Identify the blood parasite species.
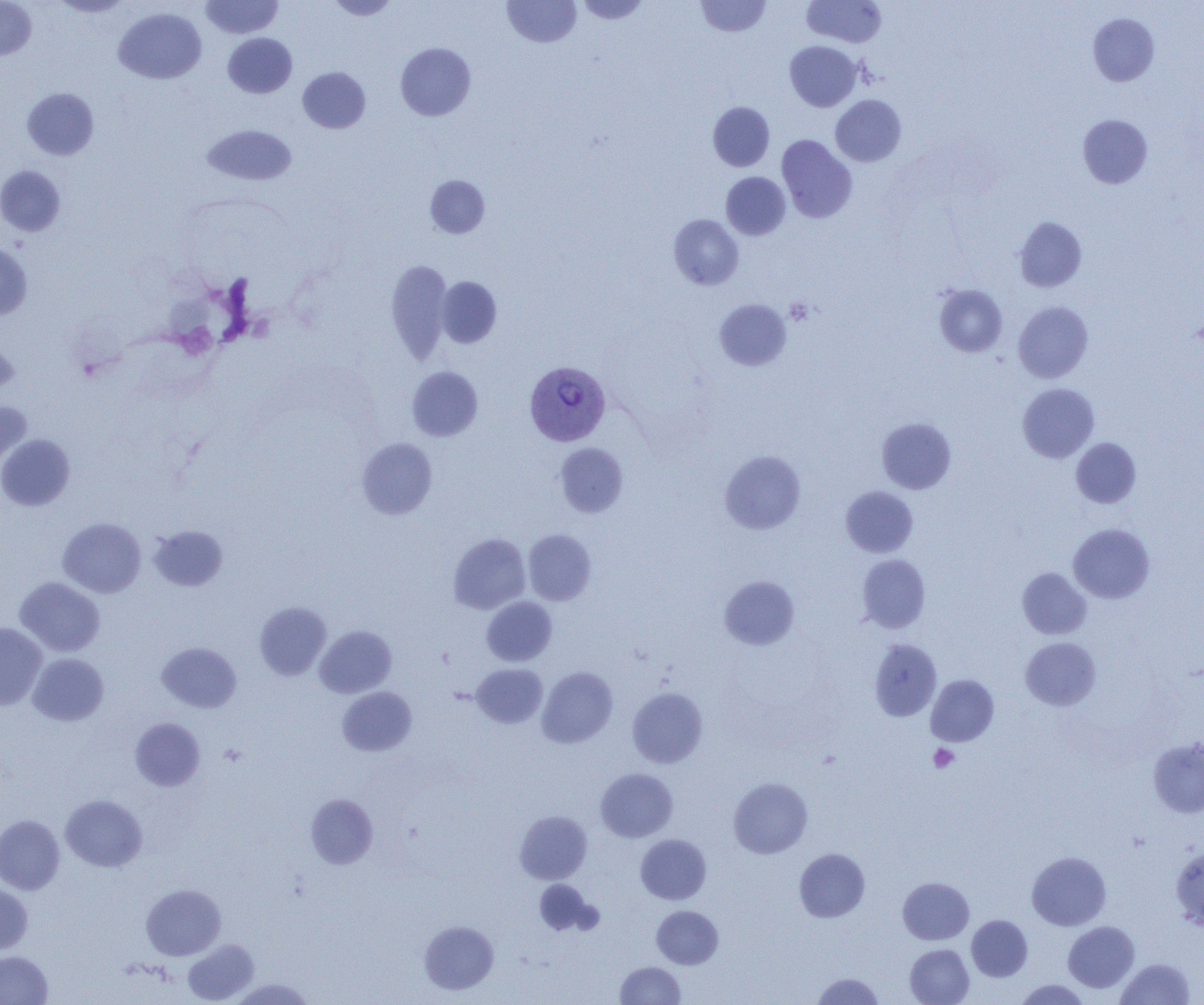
Plasmodium vivax.

Approximate bounding boxes as named x1/y1/x2/y2 corners in pixels. Platelet locations: (x1=785, y1=298, x2=813, y2=325), (x1=929, y1=744, x2=959, y2=772). Uninfected red blood cell locations: (x1=0, y1=0, x2=36, y2=60), (x1=51, y1=0, x2=132, y2=17), (x1=200, y1=0, x2=283, y2=38), (x1=326, y1=0, x2=399, y2=20), (x1=503, y1=0, x2=581, y2=47), (x1=576, y1=0, x2=649, y2=24), (x1=696, y1=0, x2=771, y2=37), (x1=802, y1=0, x2=886, y2=48), (x1=114, y1=8, x2=206, y2=84), (x1=1088, y1=13, x2=1159, y2=86), (x1=223, y1=33, x2=297, y2=98), (x1=785, y1=41, x2=861, y2=111), (x1=395, y1=42, x2=475, y2=120), (x1=298, y1=67, x2=370, y2=133), (x1=22, y1=87, x2=99, y2=160), (x1=831, y1=95, x2=906, y2=166), (x1=708, y1=102, x2=774, y2=171), (x1=1078, y1=115, x2=1152, y2=188), (x1=202, y1=124, x2=297, y2=185), (x1=777, y1=135, x2=857, y2=223), (x1=0, y1=165, x2=65, y2=236), (x1=721, y1=172, x2=790, y2=239), (x1=425, y1=175, x2=489, y2=238), (x1=669, y1=214, x2=743, y2=290), (x1=1015, y1=216, x2=1086, y2=292), (x1=0, y1=244, x2=32, y2=319), (x1=386, y1=260, x2=453, y2=363), (x1=436, y1=276, x2=502, y2=348), (x1=934, y1=285, x2=1007, y2=357), (x1=714, y1=298, x2=791, y2=371), (x1=1013, y1=301, x2=1093, y2=383), (x1=0, y1=334, x2=18, y2=398), (x1=407, y1=366, x2=483, y2=441), (x1=1017, y1=383, x2=1099, y2=462), (x1=0, y1=401, x2=32, y2=468), (x1=877, y1=418, x2=956, y2=493), (x1=0, y1=434, x2=75, y2=511), (x1=357, y1=438, x2=438, y2=519), (x1=1071, y1=438, x2=1141, y2=508), (x1=555, y1=443, x2=628, y2=517), (x1=719, y1=450, x2=806, y2=534), (x1=840, y1=486, x2=918, y2=557), (x1=58, y1=517, x2=146, y2=598), (x1=1068, y1=523, x2=1155, y2=603), (x1=149, y1=526, x2=228, y2=591), (x1=523, y1=529, x2=596, y2=605), (x1=448, y1=533, x2=530, y2=614), (x1=857, y1=554, x2=930, y2=633), (x1=1017, y1=567, x2=1092, y2=639), (x1=719, y1=576, x2=799, y2=649), (x1=15, y1=577, x2=105, y2=656), (x1=482, y1=597, x2=557, y2=666), (x1=255, y1=602, x2=331, y2=680), (x1=0, y1=622, x2=47, y2=710), (x1=314, y1=625, x2=396, y2=698), (x1=1020, y1=637, x2=1101, y2=711), (x1=869, y1=638, x2=941, y2=721), (x1=157, y1=642, x2=242, y2=713), (x1=28, y1=653, x2=109, y2=726), (x1=471, y1=663, x2=547, y2=728), (x1=537, y1=666, x2=618, y2=747), (x1=926, y1=674, x2=998, y2=746), (x1=337, y1=687, x2=417, y2=756), (x1=627, y1=687, x2=708, y2=768), (x1=130, y1=717, x2=205, y2=791), (x1=1148, y1=737, x2=1204, y2=818), (x1=596, y1=768, x2=677, y2=842), (x1=729, y1=777, x2=812, y2=858), (x1=305, y1=793, x2=378, y2=868), (x1=60, y1=795, x2=147, y2=872), (x1=514, y1=810, x2=592, y2=884), (x1=0, y1=815, x2=65, y2=894), (x1=636, y1=834, x2=711, y2=904), (x1=1171, y1=847, x2=1204, y2=930), (x1=794, y1=848, x2=870, y2=922), (x1=1027, y1=851, x2=1111, y2=930), (x1=898, y1=877, x2=974, y2=944), (x1=534, y1=879, x2=597, y2=936), (x1=0, y1=883, x2=32, y2=953), (x1=141, y1=884, x2=225, y2=960), (x1=652, y1=905, x2=723, y2=969), (x1=967, y1=915, x2=1032, y2=981), (x1=419, y1=920, x2=499, y2=994), (x1=1063, y1=921, x2=1139, y2=992), (x1=182, y1=939, x2=258, y2=1004), (x1=905, y1=944, x2=973, y2=1005), (x1=0, y1=951, x2=52, y2=1004), (x1=1116, y1=958, x2=1195, y2=1004), (x1=615, y1=961, x2=685, y2=1004), (x1=812, y1=972, x2=883, y2=1004), (x1=230, y1=978, x2=314, y2=1005), (x1=1015, y1=979, x2=1090, y2=1004). Plasmodium vivax-infected red blood cell locations: (x1=524, y1=361, x2=610, y2=446). Single field of view. Thin blood film. Captured at 1000x magnification. Optical microscopy. Image is 1204×1005 pixels.